Identify the parasite.
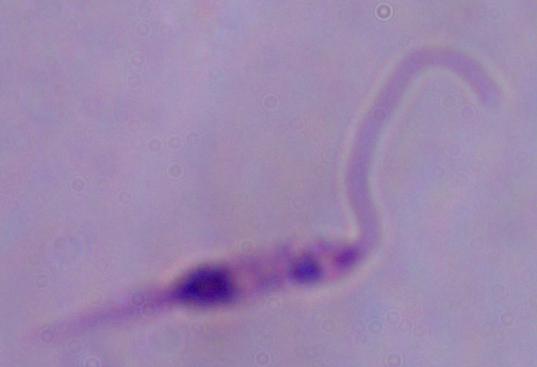
Leishmania.

modality = micrograph
magnification = 1000x